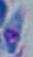
Summary:
  - Identification: Toxoplasma gondii
  - Magnification: 1000x
  - Modality: photomicrograph